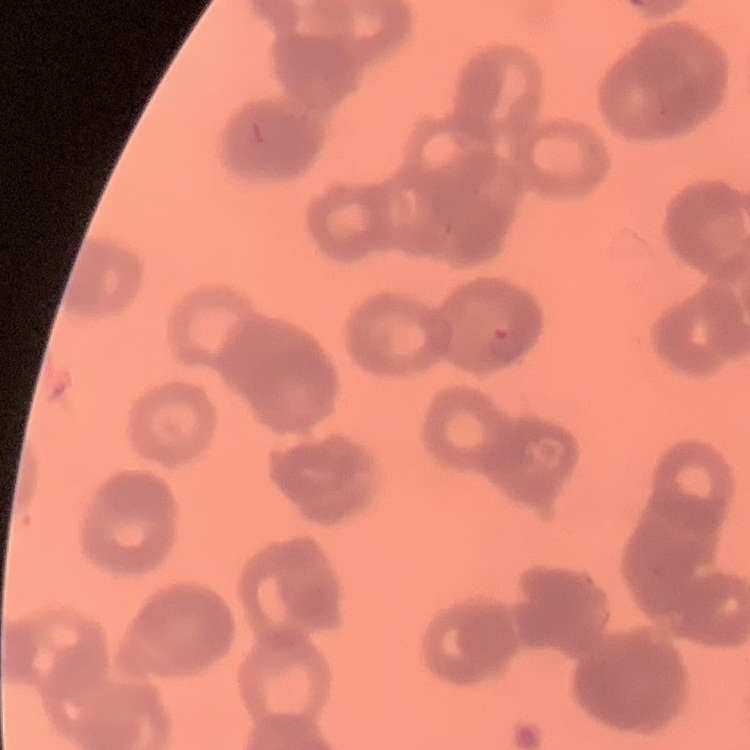

Summary:
  - Erythrocyte morphology: rouleaux formation
  - Stain: Field's or Giemsa
  - Preparation: thin blood film
  - Image type: square crop of a larger photomicrograph